Assess this cell for malaria.
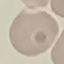
It is uninfected.

Summary:
  - Image type: cell patch, automatically extracted from a larger field of view and resized to 64 × 64 pixels
  - Stain: Giemsa
  - Preparation: thin smear
  - Capture: smartphone through the microscope eyepiece